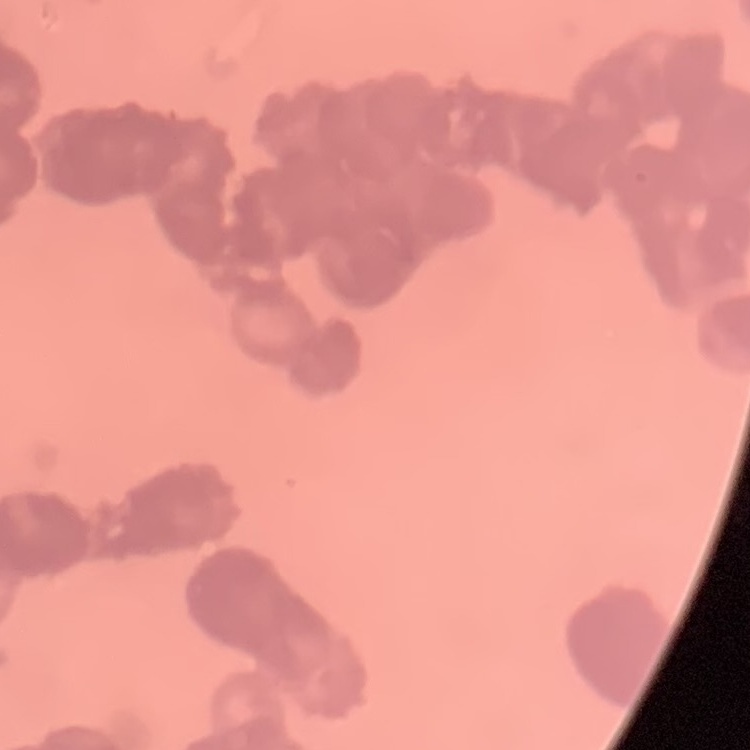
Summary:
  - Red blood cell morphology: rouleaux formation
  - Image type: one tile cut from a larger photomicrograph
  - Preparation: thin blood smear
  - Stain: Field's or Giemsa